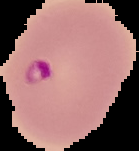

result = Plasmodium parasites detected
preparation = thin blood film
image type = segmented cell region with the area outside set to black
image size = 139×151 pixels